Point out each malaria parasite.
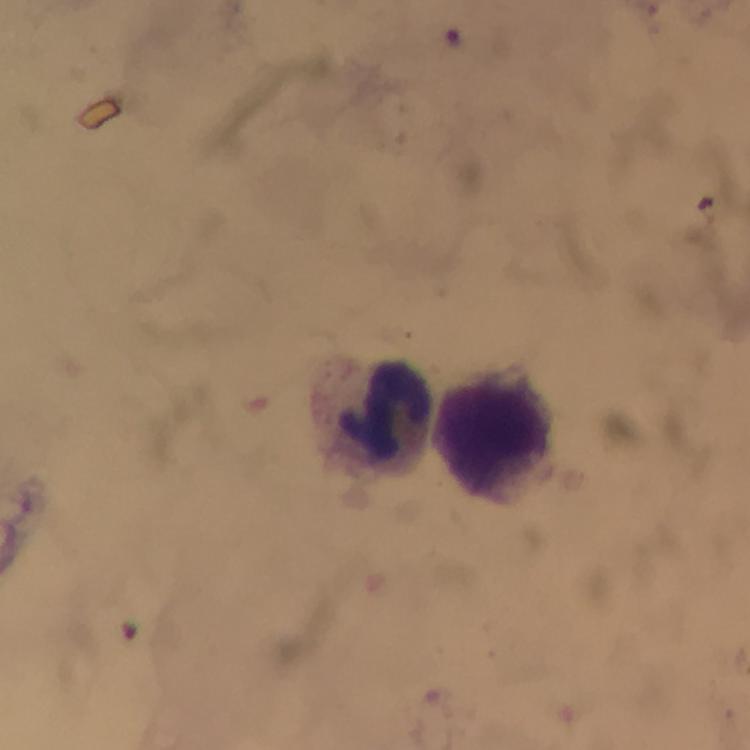
No malaria parasites detected.

image size = 750×750 pixels
leukocyte locations = approximate centers as (x, y) in pixels: (372, 412), (494, 436)
capture = smartphone mounted on the microscope
preparation = thick blood smear
stain = Giemsa
context = from a diagnostic examination for malaria
immersion oil = used
cropped from = one field of view
magnification = 100x